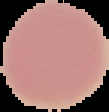
Summary:
  - Result: negative for Plasmodium parasites
  - Preparation: thin blood film
  - Image size: 109×112 pixels
  - Image type: segmented cell region on a black background